State which cell type is depicted.
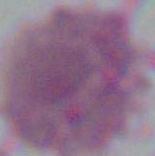

This is an erythrocyte.

Summary:
  - Magnification: 1000x
  - Modality: micrograph